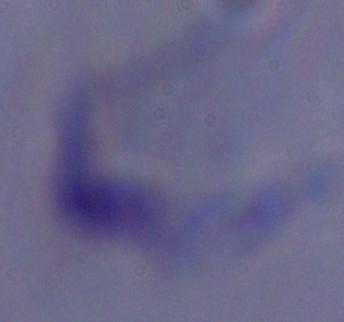
magnification = 1000x
identification = trypanosome
modality = photomicrograph